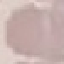 Malaria status: uninfected. Thin blood film. Giemsa stain. Automatically extracted cell patch, resized to 64 × 64 pixels. Acquired by smartphone through the microscope eyepiece.